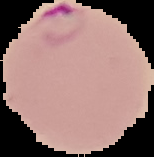

image size = 154×157 pixels
image type = segmented cell region on a black background
malaria status = parasitized
preparation = thin blood film